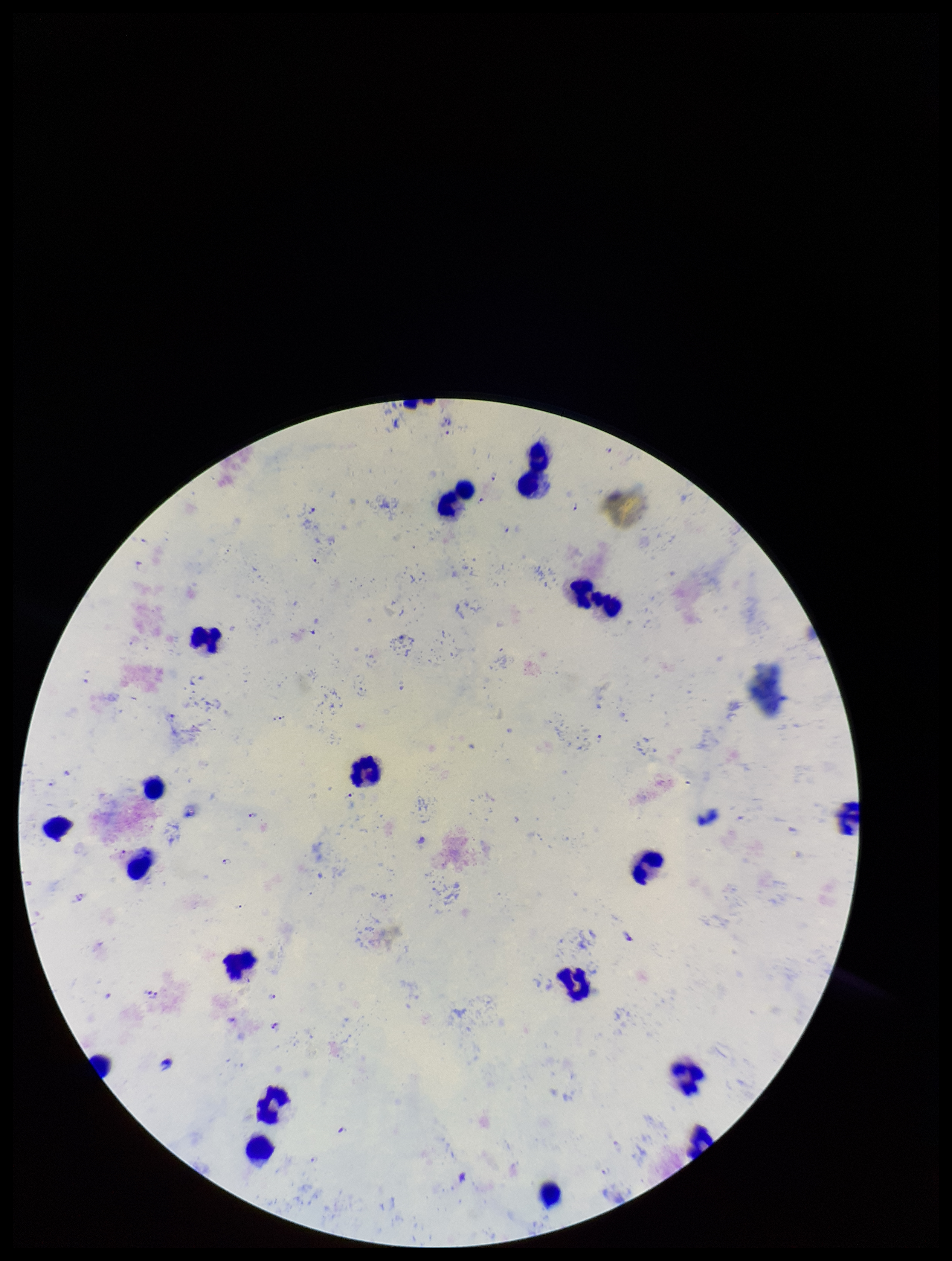

{
  "stain": "Giemsa",
  "preparation": "thick blood smear",
  "plasmodium_parasites": "identified",
  "field_of_view": "single",
  "image_size": "952×1261 pixels",
  "capture": "smartphone photograph through the microscope eyepiece",
  "leukocyte_count": 20,
  "species_reported_for_this_patient": "Plasmodium falciparum",
  "patient_malaria_status": "infected",
  "parasite_count": 24
}